Report the malaria status of this cell.
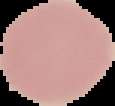
It is uninfected.

image_type: cell region segmented out of the field of view; surrounding area masked to black
image_size: 115×106 pixels
preparation: thin blood smear